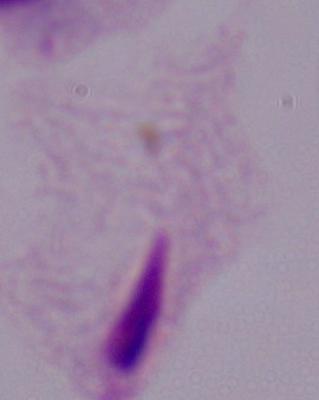

magnification = 1000x
identification = trichomonad
modality = photomicrograph